Classify this cell by malaria status.
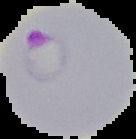
Parasitized.

Summary:
  - Preparation: thin blood smear
  - Image size: 136×139 pixels
  - Image type: segmented cell region with the area outside set to black